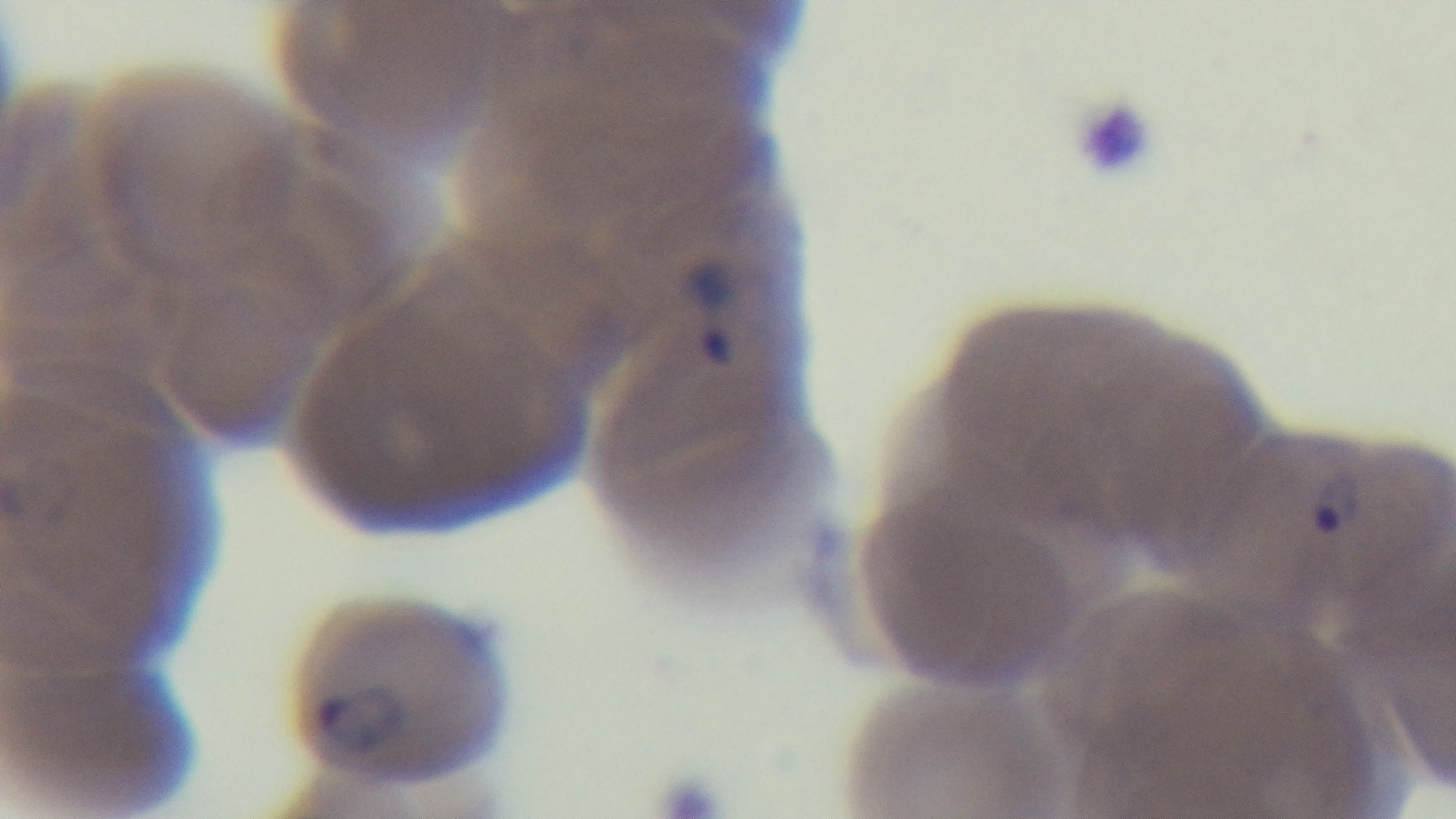

field of view = one from the slide
objective = 100x oil immersion
stain = Giemsa
malaria status = infected
capture = mounted 4K digital camera
modality = light microscopy
preparation = thin smear